Describe the morphology of the red blood cells.
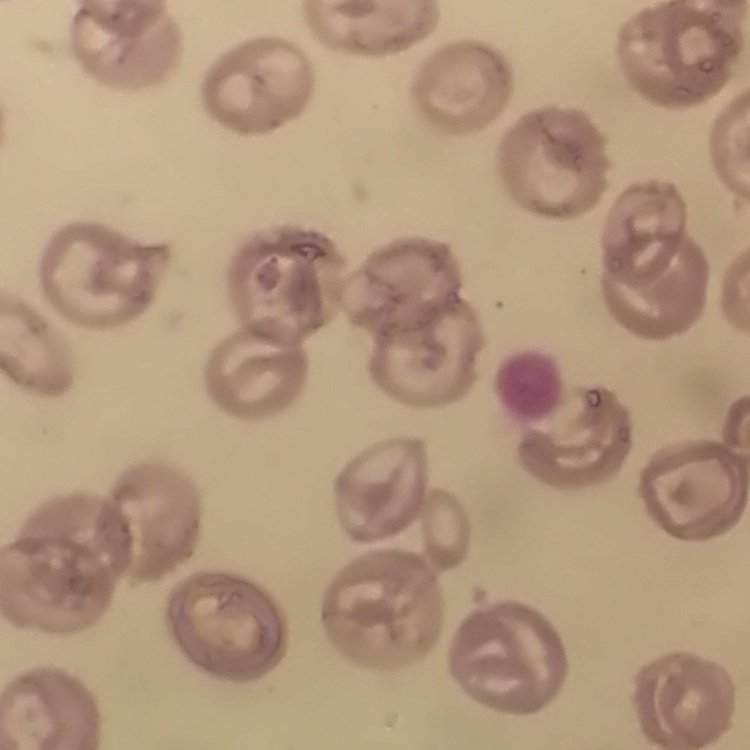

No rouleaux formation.

Summary:
  - Image type: square crop of a larger photomicrograph
  - Stain: Field's or Giemsa
  - Preparation: thin blood smear